Identify the parasite.
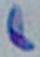
Toxoplasma gondii.

1000x magnification. Photomicrograph.